Give the extent of all Trypanosoma brucei.
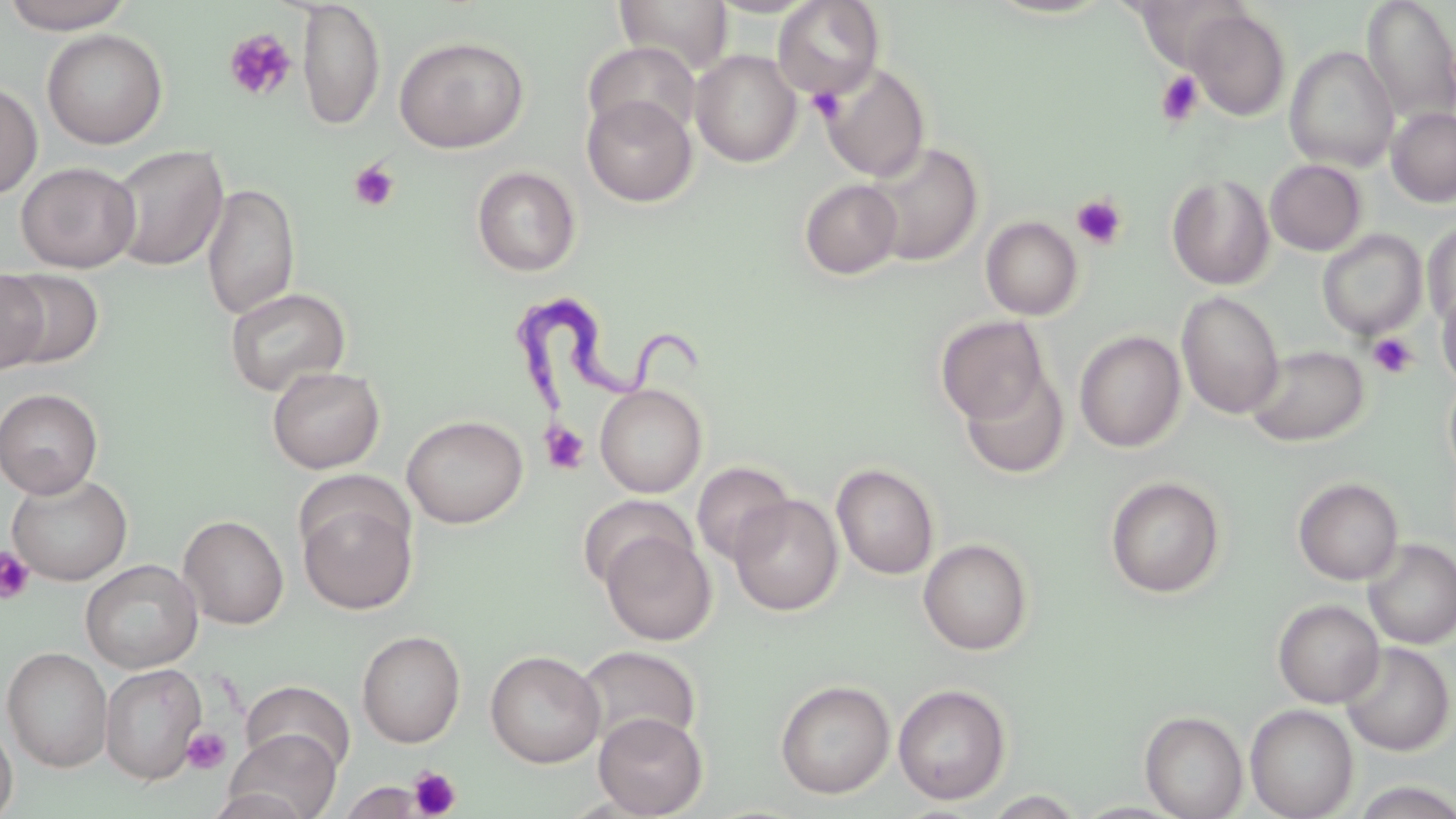
Approximate bounding boxes as (x1,y1)-(x2,y2) corner pairs in pixels.
Trypanosoma brucei: (521,289)-(702,423).

Summary:
  - Uninfected red blood cell locations: (614,0)-(733,74), (772,0)-(885,99), (1131,0)-(1253,71), (1361,0)-(1456,123), (1,1)-(137,34), (297,1)-(386,132), (1185,8)-(1291,121), (42,29)-(168,149), (394,35)-(530,153), (583,41)-(701,142), (1284,46)-(1399,171), (690,49)-(802,167), (821,63)-(930,182), (0,80)-(43,199), (582,94)-(698,207), (1387,107)-(1456,207), (861,141)-(984,267), (107,144)-(229,272), (1265,159)-(1367,256), (15,161)-(141,272), (471,165)-(581,277), (1167,173)-(1275,290), (799,179)-(903,280), (201,182)-(300,319), (980,215)-(1084,320), (1422,222)-(1456,328), (1316,229)-(1428,340), (3,268)-(103,370), (0,269)-(49,375), (1436,283)-(1456,392), (224,286)-(351,397), (1176,291)-(1285,419), (935,315)-(1051,425), (1074,330)-(1187,452), (1246,344)-(1370,447), (266,366)-(385,474), (958,366)-(1070,479), (1443,373)-(1456,484), (595,383)-(707,498), (0,388)-(103,499), (402,414)-(528,528), (692,461)-(795,565), (831,463)-(939,579), (6,473)-(133,585), (1104,475)-(1226,598), (1293,477)-(1404,585), (296,487)-(419,615), (578,493)-(695,591), (730,494)-(843,616), (178,514)-(289,629), (602,528)-(715,646), (918,537)-(1034,654), (1362,538)-(1456,649), (81,559)-(203,673), (1272,599)-(1385,708), (357,630)-(466,747), (1340,642)-(1455,756), (2,646)-(113,773), (575,646)-(702,752), (485,650)-(605,768), (100,663)-(206,785), (240,680)-(356,777), (775,680)-(895,799), (892,683)-(1012,805), (1245,704)-(1358,818), (1140,710)-(1248,818), (593,712)-(708,818), (0,718)-(18,819), (224,729)-(342,819), (339,780)-(428,818), (1349,780)-(1456,819), (204,788)-(314,819), (981,790)-(1088,818)
  - Platelet locations: (223,28)-(297,102), (1156,70)-(1204,126), (807,87)-(845,125), (347,160)-(400,212), (1071,194)-(1127,250), (1368,332)-(1418,378), (541,422)-(590,474), (1,547)-(35,603), (182,727)-(231,775), (410,766)-(461,818)
  - Slide-level diagnosis: Trypanosoma brucei
  - Preparation: thin blood smear
  - Stain: May-Grünwald-Giemsa
  - Modality: optical microscopy
  - Image size: 1456×819 pixels
  - Field of view: single
  - Magnification: 1000x